Classify this cell by malaria status.
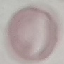
It is uninfected.

Giemsa-stained preparation. Thin smear of blood. Photographed with a smartphone camera at the microscope eyepiece. Cell patch, automatically extracted from a larger field of view and resized to 64 × 64 pixels.